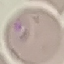 Result: malaria parasites identified. Acquired by smartphone through the microscope eyepiece. Thin smear of blood. Automatically extracted cell patch, resized to 64 × 64 pixels. Giemsa-stained preparation.